Give the position of every leukocyte visible.
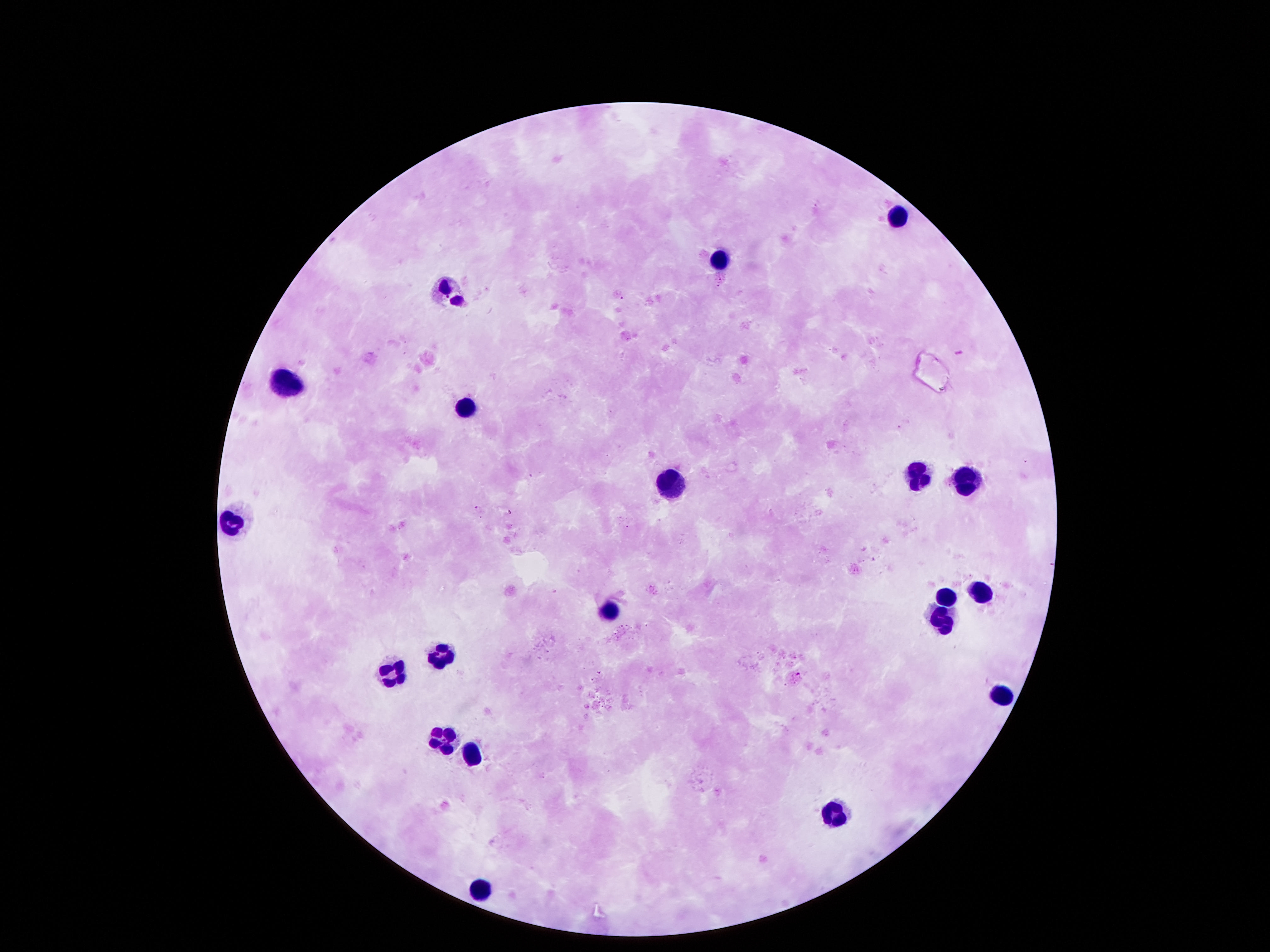

Approximate centers as (x, y) in pixels.
Leukocytes: (901, 215), (720, 259), (451, 288), (290, 379), (458, 412), (918, 473), (965, 473), (666, 477), (230, 524), (982, 590), (945, 591), (609, 608), (935, 623), (441, 655), (394, 674), (1002, 692), (441, 741), (478, 751), (838, 811), (478, 890).

Summary:
  - Stain: Giemsa
  - Preparation: thick blood smear
  - Magnification: 100x
  - Capture: smartphone camera through the microscope eyepiece
  - Patient malaria status: negative
  - Image size: 1270×952 pixels
  - Field of view: one from this slide